Name the parasite shown.
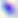
This is Toxoplasma gondii.

Summary:
  - Magnification: 400x
  - Modality: photomicrograph